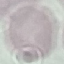
malaria status = uninfected
image type = automatically extracted cell patch, resized to 64 × 64 pixels
preparation = thin blood smear
stain = Giemsa
capture = smartphone through the microscope eyepiece